Give the preparation type.
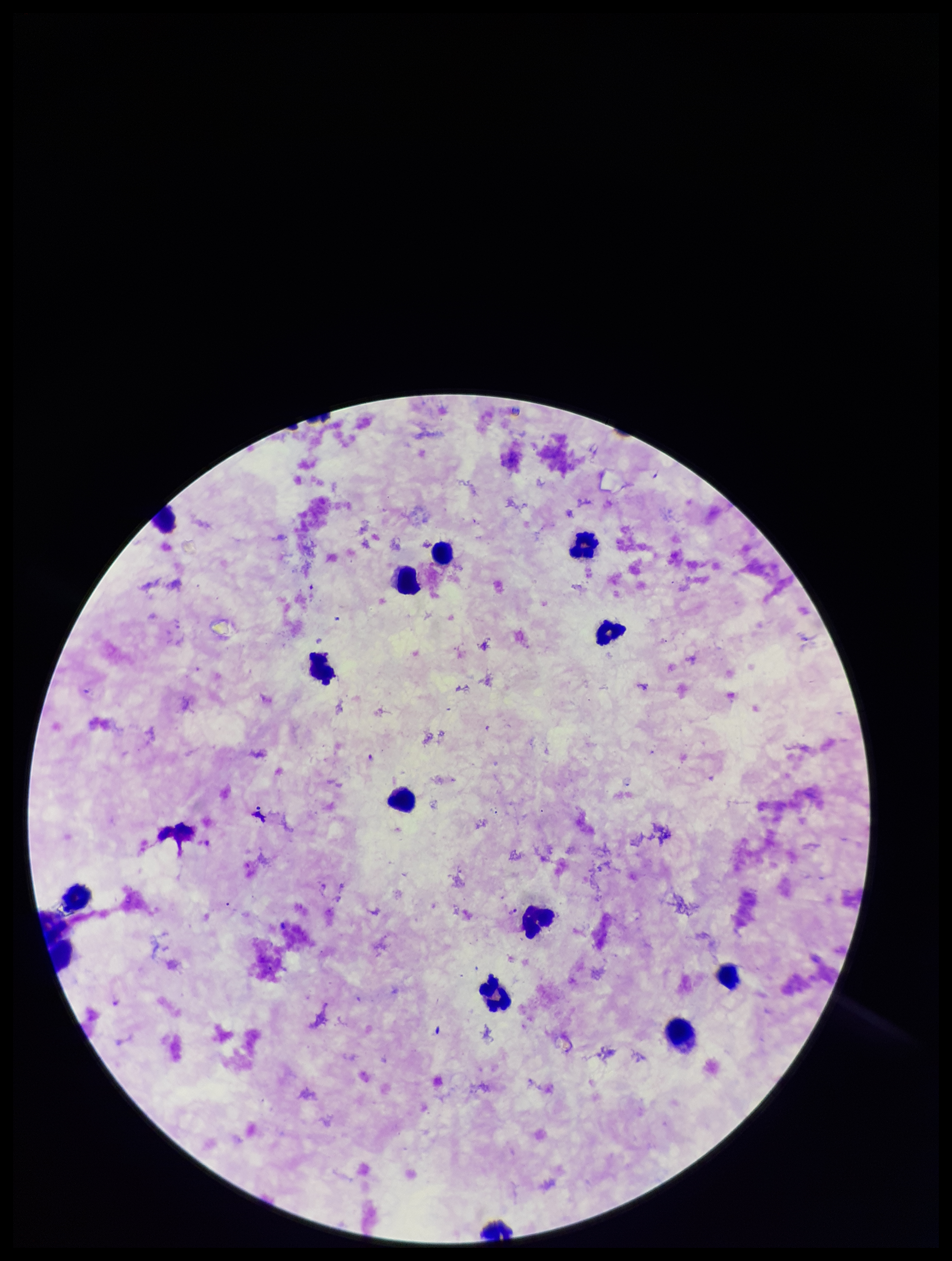
Thick.

Summary:
  - Capture: smartphone photograph through the microscope eyepiece
  - Species reported for this patient: Plasmodium falciparum
  - Leukocyte count: 13
  - Field of view: one from this slide
  - Stain: Giemsa
  - Image size: 952×1261 pixels
  - Plasmodium parasites: seen
  - Patient malaria status: positive
  - Parasite count: 2